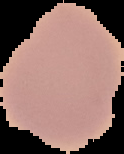
malaria status = uninfected
image type = segmented cell region on a black background
preparation = thin blood film
image size = 124×154 pixels